Outline platelets.
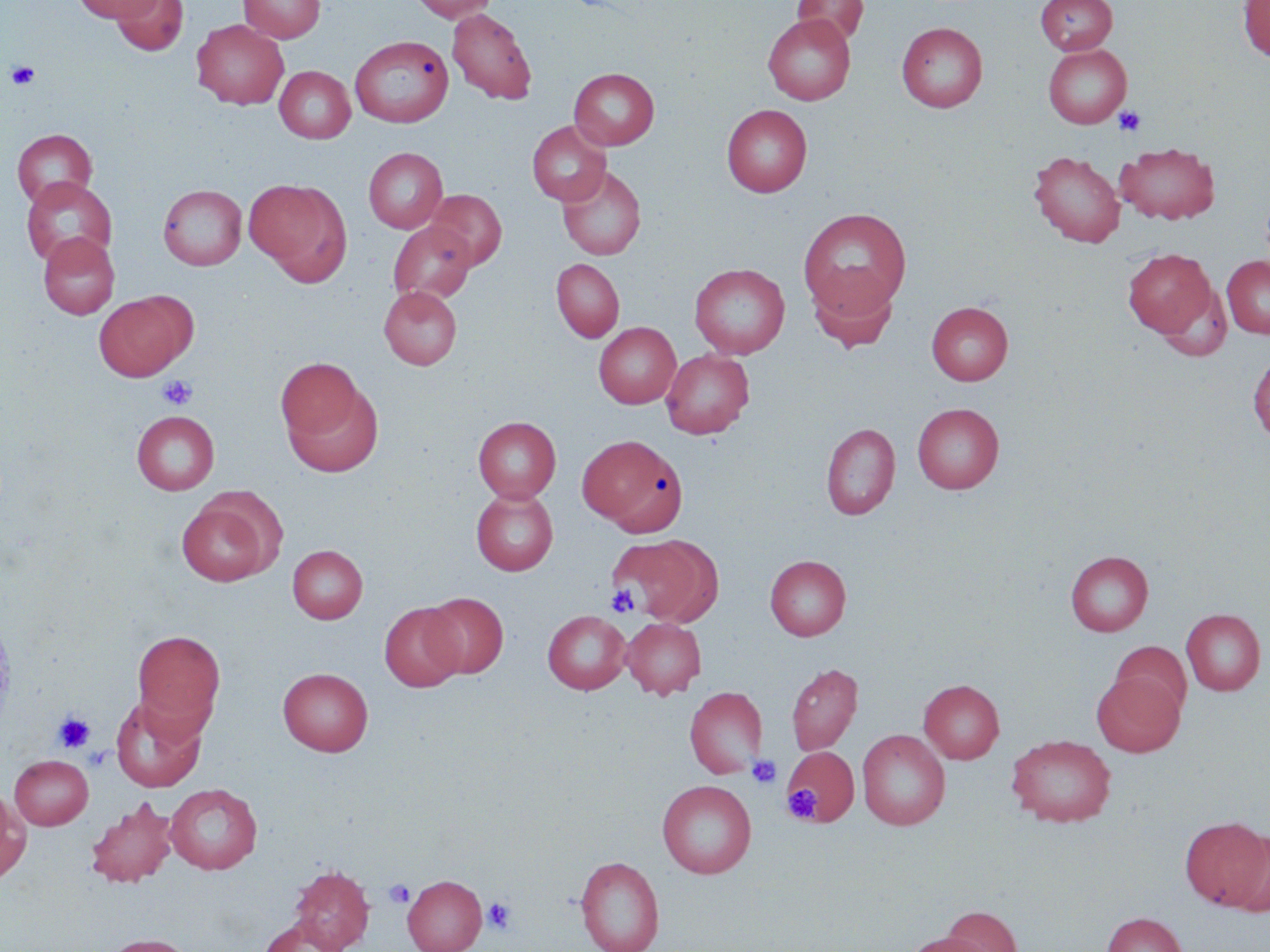
Approximate bounding boxes as (x1,y1)-(x2,y2) corner pairs in pixels.
Platelets: (6,61)-(40,89), (1113,106)-(1146,136), (157,375)-(197,410), (607,584)-(640,617), (53,712)-(94,752), (781,748)-(857,826), (747,755)-(782,789), (782,784)-(821,823), (384,879)-(414,908), (482,897)-(516,934).

Summary:
  - Uninfected red blood cell locations: (73,0)-(163,22), (239,0)-(325,43), (408,0)-(499,22), (1035,0)-(1117,55), (1238,0)-(1270,62), (112,1)-(188,57), (792,1)-(869,46), (447,8)-(537,105), (763,13)-(855,105), (192,19)-(288,109), (897,21)-(988,112), (350,36)-(452,127), (1043,43)-(1132,128), (275,65)-(355,143), (569,68)-(660,150), (722,104)-(812,197), (527,121)-(611,206), (12,129)-(98,208), (1116,142)-(1219,225), (363,147)-(448,233), (1028,150)-(1125,247), (557,165)-(646,260), (21,176)-(117,268), (244,178)-(351,283), (158,184)-(246,270), (425,189)-(507,270), (797,207)-(912,319), (388,221)-(476,303), (38,232)-(119,319), (1123,247)-(1217,338), (1222,256)-(1270,338), (551,259)-(624,342), (689,263)-(790,359), (807,268)-(899,352), (379,286)-(461,369), (94,291)-(195,381), (927,301)-(1013,385), (593,322)-(681,408), (661,349)-(754,439), (1248,353)-(1270,444), (276,358)-(364,442), (283,380)-(384,477), (912,403)-(1003,494), (132,411)-(219,495), (473,417)-(561,503), (821,423)-(900,520), (578,435)-(686,535), (470,489)-(558,576), (175,495)-(278,586), (612,534)-(718,625), (288,545)-(367,623), (1065,551)-(1153,636), (765,555)-(851,640), (422,592)-(508,677), (379,603)-(465,691), (1181,609)-(1266,696), (542,610)-(631,694), (622,617)-(706,699), (132,629)-(226,733), (1110,641)-(1191,717), (786,662)-(862,755), (277,667)-(373,756), (1091,672)-(1184,756), (919,679)-(1004,763), (676,684)-(762,876), (685,686)-(768,778), (110,694)-(207,791), (857,729)-(950,830), (1007,734)-(1116,827), (784,747)-(859,824), (9,754)-(93,829), (657,779)-(756,878), (165,783)-(262,874), (0,785)-(31,885), (86,797)-(179,888), (1180,817)-(1269,910), (1226,831)-(1270,917), (575,855)-(665,952), (288,864)-(375,951), (403,874)-(487,952), (940,906)-(1022,952), (1102,912)-(1188,952), (257,917)-(347,951), (901,932)-(994,952), (101,933)-(196,952)
  - Slide-level diagnosis: negative for blood parasites
  - Preparation: thin blood film
  - Field of view: one of a larger specimen
  - Magnification: 1000x
  - Modality: optical microscopy
  - Image size: 1270×952 pixels
  - Stain: May-Grünwald-Giemsa